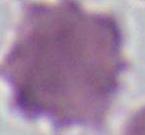
{
  "modality": "micrograph",
  "magnification": "1000x",
  "identification": "red blood cell"
}